Outline platelets.
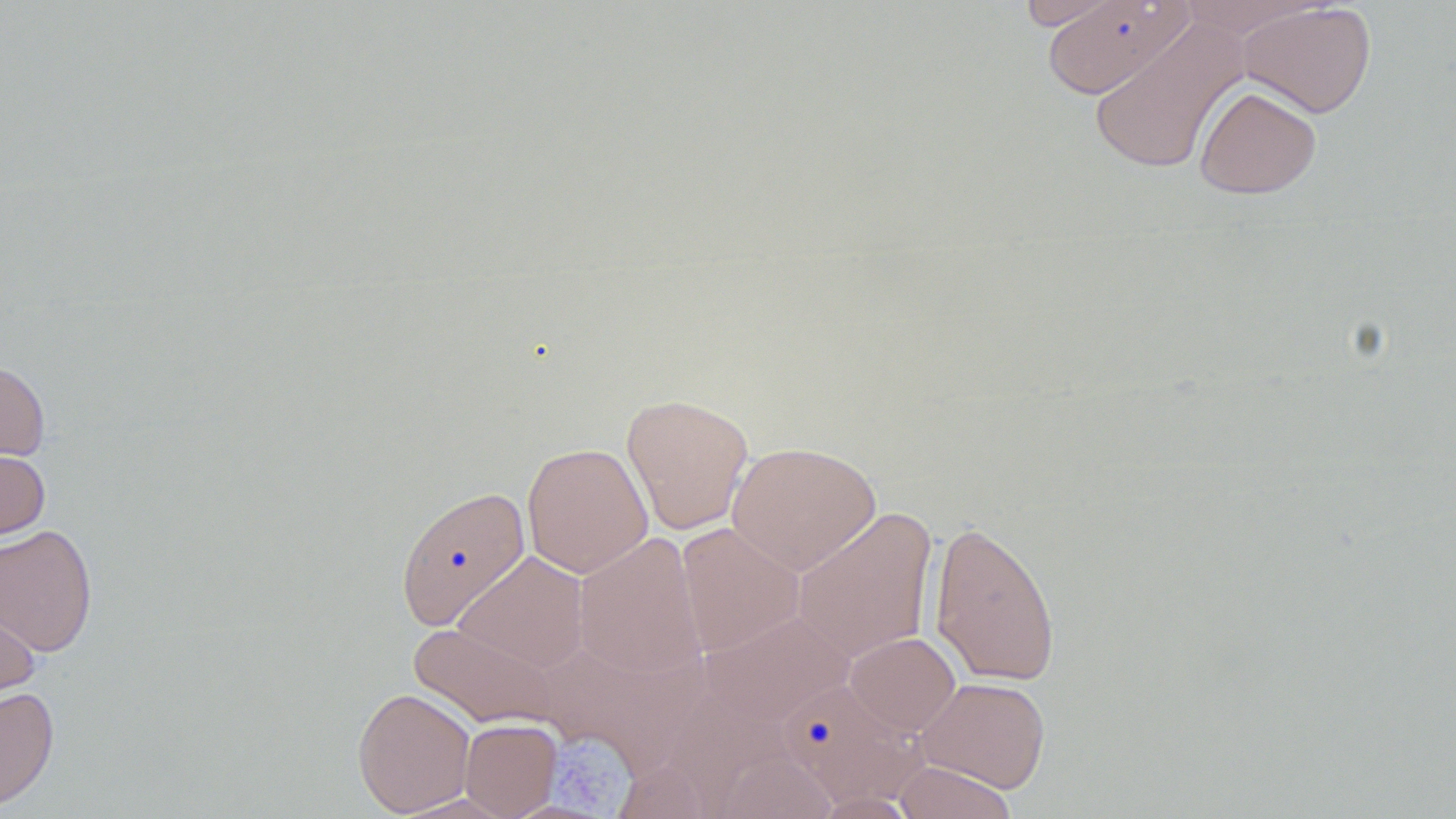

Approximate bounding boxes as named x1/y1/x2/y2 corners in pixels.
Platelets: (x1=552, y1=740, x2=640, y2=817).

Summary:
  - Uninfected red blood cell locations: (x1=1015, y1=0, x2=1130, y2=29), (x1=1047, y1=0, x2=1198, y2=97), (x1=1176, y1=0, x2=1328, y2=39), (x1=1237, y1=2, x2=1377, y2=118), (x1=1088, y1=19, x2=1248, y2=175), (x1=1194, y1=85, x2=1322, y2=199), (x1=0, y1=358, x2=51, y2=466), (x1=621, y1=393, x2=754, y2=535), (x1=522, y1=441, x2=653, y2=578), (x1=726, y1=441, x2=880, y2=575), (x1=0, y1=448, x2=50, y2=540), (x1=395, y1=484, x2=531, y2=631), (x1=792, y1=507, x2=938, y2=663), (x1=929, y1=519, x2=1061, y2=687), (x1=0, y1=523, x2=98, y2=656), (x1=676, y1=523, x2=805, y2=658), (x1=572, y1=532, x2=708, y2=682), (x1=454, y1=550, x2=590, y2=674), (x1=0, y1=603, x2=40, y2=713), (x1=699, y1=610, x2=856, y2=727), (x1=409, y1=621, x2=563, y2=730), (x1=845, y1=631, x2=960, y2=737), (x1=916, y1=676, x2=1051, y2=793), (x1=781, y1=678, x2=925, y2=807), (x1=0, y1=686, x2=59, y2=811), (x1=352, y1=686, x2=476, y2=817), (x1=459, y1=718, x2=562, y2=818), (x1=714, y1=751, x2=840, y2=819), (x1=892, y1=761, x2=1018, y2=819), (x1=809, y1=792, x2=922, y2=818)
  - Slide-level diagnosis: no evidence of blood parasites
  - Image size: 1456×819 pixels
  - Stain: May-Grünwald-Giemsa
  - Magnification: 1000x
  - Preparation: thin blood film
  - Field of view: one of a larger specimen
  - Modality: light microscopy